Identify the parasite.
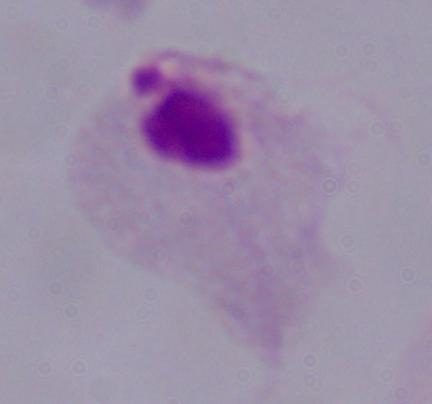

This is a trichomonad.

Captured at 1000x magnification. Micrograph.